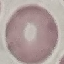 Malaria status: uninfected. Cell patch, automatically extracted from a larger field of view and resized to 64 × 64 pixels. Thin blood film. Acquired by smartphone through the microscope eyepiece. Giemsa-stained preparation.